Give the extent of all Plasmodium falciparum-infected red blood cells.
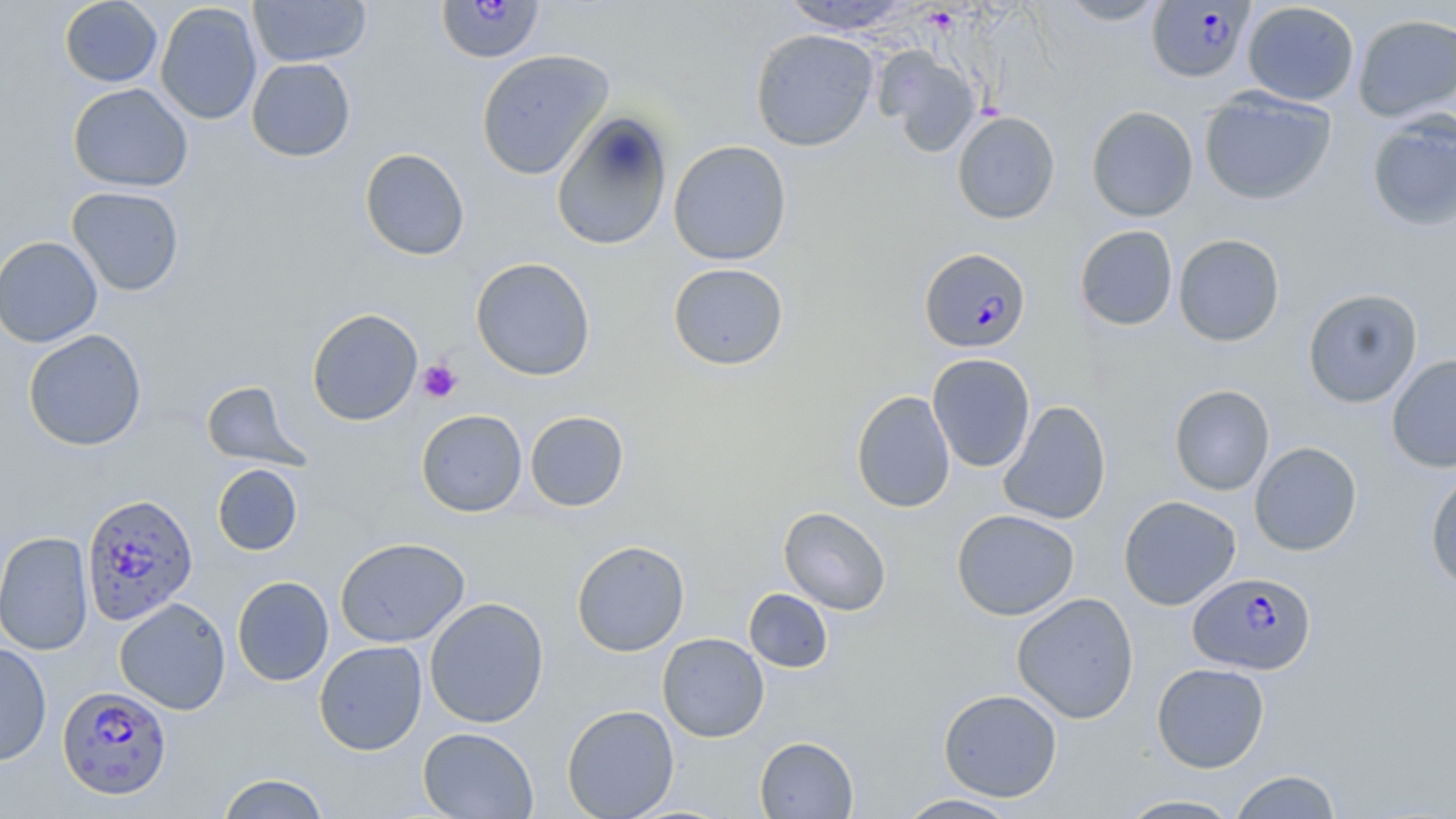

Approximate bounding boxes as named x1/y1/x2/y2 corners in pixels.
Plasmodium falciparum-infected red blood cells: (x1=436, y1=0, x2=545, y2=63), (x1=1147, y1=1, x2=1255, y2=84), (x1=919, y1=247, x2=1031, y2=353), (x1=82, y1=492, x2=198, y2=630), (x1=1188, y1=571, x2=1316, y2=675), (x1=58, y1=685, x2=172, y2=799).

Uninfected red blood cell locations: (x1=59, y1=0, x2=162, y2=87), (x1=248, y1=0, x2=371, y2=67), (x1=1055, y1=0, x2=1170, y2=26), (x1=779, y1=1, x2=914, y2=35), (x1=1242, y1=1, x2=1360, y2=106), (x1=155, y1=2, x2=262, y2=125), (x1=1352, y1=13, x2=1456, y2=122), (x1=750, y1=29, x2=878, y2=151), (x1=475, y1=49, x2=614, y2=180), (x1=877, y1=49, x2=982, y2=157), (x1=246, y1=58, x2=356, y2=162), (x1=67, y1=83, x2=193, y2=192), (x1=1199, y1=88, x2=1337, y2=206), (x1=1086, y1=105, x2=1198, y2=222), (x1=551, y1=110, x2=673, y2=252), (x1=952, y1=111, x2=1060, y2=224), (x1=1366, y1=111, x2=1456, y2=233), (x1=667, y1=140, x2=791, y2=265), (x1=359, y1=148, x2=470, y2=261), (x1=66, y1=186, x2=185, y2=296), (x1=1074, y1=225, x2=1179, y2=331), (x1=1173, y1=233, x2=1286, y2=347), (x1=0, y1=236, x2=103, y2=348), (x1=470, y1=257, x2=596, y2=381), (x1=668, y1=262, x2=789, y2=370), (x1=1302, y1=288, x2=1423, y2=408), (x1=306, y1=308, x2=423, y2=426), (x1=23, y1=329, x2=147, y2=451), (x1=927, y1=353, x2=1036, y2=473), (x1=1387, y1=353, x2=1456, y2=472), (x1=201, y1=380, x2=308, y2=470), (x1=1169, y1=384, x2=1274, y2=495), (x1=851, y1=391, x2=956, y2=513), (x1=997, y1=400, x2=1112, y2=525), (x1=416, y1=409, x2=528, y2=516), (x1=525, y1=410, x2=630, y2=511), (x1=1249, y1=442, x2=1362, y2=556), (x1=212, y1=463, x2=303, y2=556), (x1=1425, y1=469, x2=1456, y2=592), (x1=1118, y1=495, x2=1241, y2=610), (x1=779, y1=507, x2=891, y2=615), (x1=951, y1=509, x2=1080, y2=621), (x1=0, y1=531, x2=94, y2=655), (x1=334, y1=537, x2=470, y2=648), (x1=571, y1=539, x2=690, y2=657), (x1=232, y1=576, x2=334, y2=686), (x1=744, y1=588, x2=833, y2=673), (x1=1011, y1=592, x2=1139, y2=724), (x1=114, y1=597, x2=231, y2=715), (x1=424, y1=597, x2=549, y2=728), (x1=657, y1=633, x2=769, y2=742), (x1=314, y1=641, x2=428, y2=755), (x1=0, y1=642, x2=52, y2=767), (x1=1151, y1=662, x2=1270, y2=773), (x1=938, y1=688, x2=1063, y2=802), (x1=562, y1=704, x2=679, y2=819), (x1=417, y1=726, x2=539, y2=819), (x1=754, y1=736, x2=858, y2=818), (x1=1229, y1=769, x2=1343, y2=818), (x1=217, y1=773, x2=331, y2=818), (x1=893, y1=793, x2=1025, y2=818), (x1=1115, y1=794, x2=1244, y2=818). Platelet locations: (x1=417, y1=359, x2=462, y2=404). Slide-level diagnosis: Plasmodium falciparum. Light microscopy. Image is 1456×819 pixels. Thin blood smear. Captured at 1000x magnification. May-Grünwald-Giemsa stain. Single field of view.